Name the cell type shown.
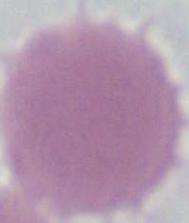
An erythrocyte.

modality = photomicrograph
magnification = 1000x